Report the malaria status of this cell.
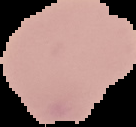

Uninfected.

The area outside the segmented cell region is set to black. From a thin blood smear. Image is 136×127 pixels.